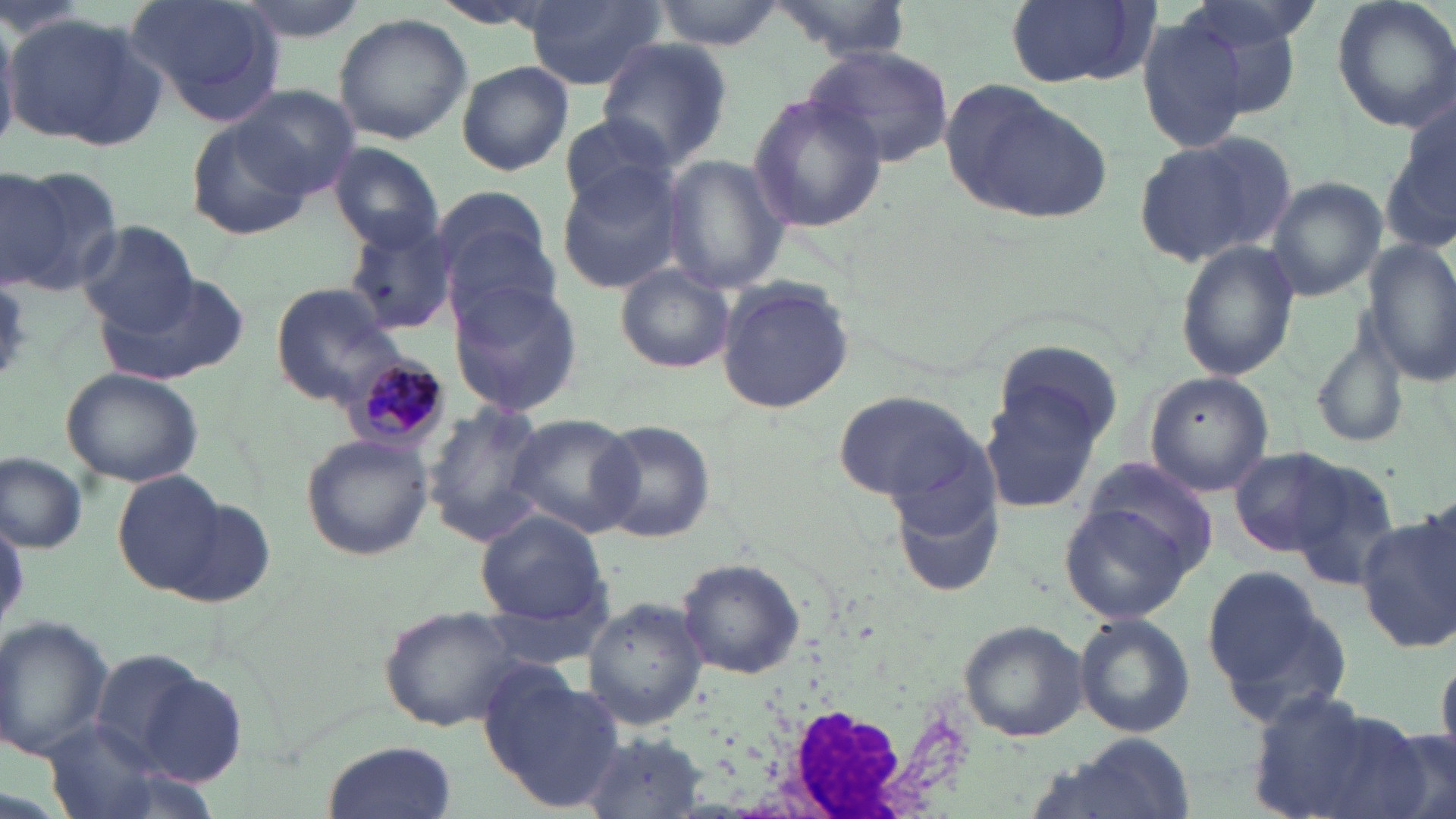
Approximate bounding boxes as (x1, y1, x2, y2) in pixels. Uninfected red blood cell locations: (117, 0, 288, 123), (230, 0, 370, 45), (653, 0, 782, 51), (1002, 0, 1158, 88), (1166, 0, 1310, 115), (1329, 0, 1456, 135), (525, 2, 661, 90), (764, 2, 915, 61), (4, 13, 166, 150), (331, 13, 473, 144), (1136, 14, 1254, 155), (594, 38, 733, 166), (804, 44, 957, 169), (457, 62, 574, 176), (939, 80, 1112, 223), (234, 85, 360, 198), (745, 90, 886, 234), (1380, 110, 1456, 259), (556, 113, 681, 213), (185, 114, 311, 238), (1134, 129, 1295, 268), (328, 144, 444, 250), (659, 155, 789, 294), (0, 164, 119, 294), (556, 166, 686, 295), (1266, 176, 1387, 300), (431, 185, 557, 312), (341, 218, 456, 337), (76, 219, 196, 332), (1175, 239, 1299, 381), (1363, 240, 1456, 381), (615, 264, 736, 374), (111, 272, 249, 383), (447, 276, 584, 416), (715, 276, 855, 416), (271, 280, 409, 407), (1308, 329, 1409, 450), (991, 336, 1124, 455), (61, 367, 205, 488), (1148, 373, 1277, 497), (980, 384, 1107, 519), (830, 387, 992, 507), (420, 402, 552, 546), (503, 413, 640, 536), (588, 418, 716, 542), (301, 432, 434, 561), (1228, 445, 1354, 556), (0, 451, 88, 553), (1079, 456, 1221, 580), (1286, 457, 1401, 587), (892, 469, 1008, 597), (114, 471, 231, 594), (1058, 496, 1200, 623), (166, 498, 276, 607), (1355, 507, 1456, 653), (476, 510, 611, 628), (676, 558, 805, 682), (1201, 565, 1347, 726), (585, 599, 706, 728), (380, 607, 525, 731), (1073, 613, 1196, 737), (0, 615, 112, 763), (960, 620, 1090, 742), (1433, 649, 1456, 770), (95, 652, 241, 783), (481, 668, 627, 814), (1243, 691, 1432, 819), (42, 722, 174, 818), (582, 732, 709, 819), (323, 737, 457, 818), (1020, 737, 1199, 819). White blood cell locations: (753, 658, 954, 819). Plasmodium malariae-infected red blood cell locations: (348, 354, 448, 447). Slide-level diagnosis: Plasmodium malariae. Single field of view. Thin blood film. Optical microscopy. Captured at 1000x magnification. Image is 1456×819 pixels. May-Grünwald-Giemsa-stained preparation.